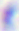
Toxoplasma gondii is seen. Photomicrograph. 400x magnification.